State which parasite is depicted.
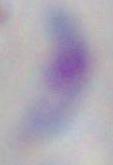

Toxoplasma gondii.

magnification = 1000x
modality = micrograph